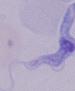

Summary:
  - Modality: micrograph
  - Magnification: 1000x
  - Identification: trypanosome